Report the malaria status of this cell.
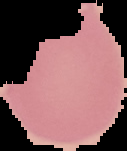
It is uninfected.

image type = cell region segmented out of the field of view; surrounding area masked to black
image size = 127×151 pixels
preparation = thin blood film